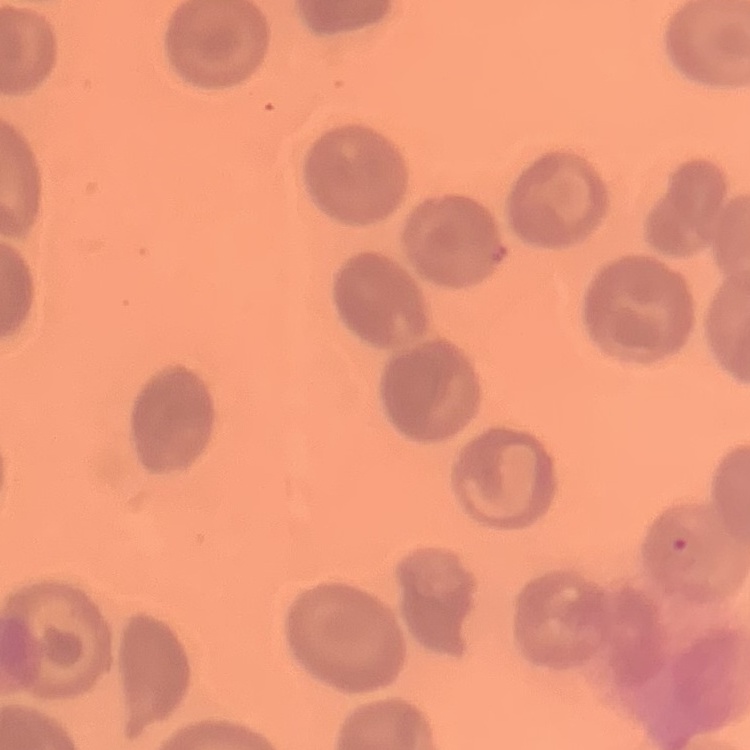 The erythrocytes exhibit no rouleaux formation. One tile cut from a larger photomicrograph. Thin blood smear. Field's or Giemsa stain.